Report the malaria status of this cell.
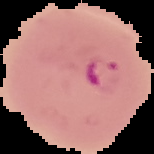

Parasitized.

Summary:
  - Image size: 154×154 pixels
  - Image type: segmented cell region on a black background
  - Preparation: thin blood smear